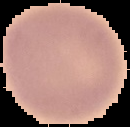
Summary:
  - Image type: segmented cell region with the area outside set to black
  - Preparation: thin blood film
  - Image size: 130×127 pixels
  - Result: no Plasmodium parasites seen